Give the extent of all Plasmodium vivax-infected red blood cells.
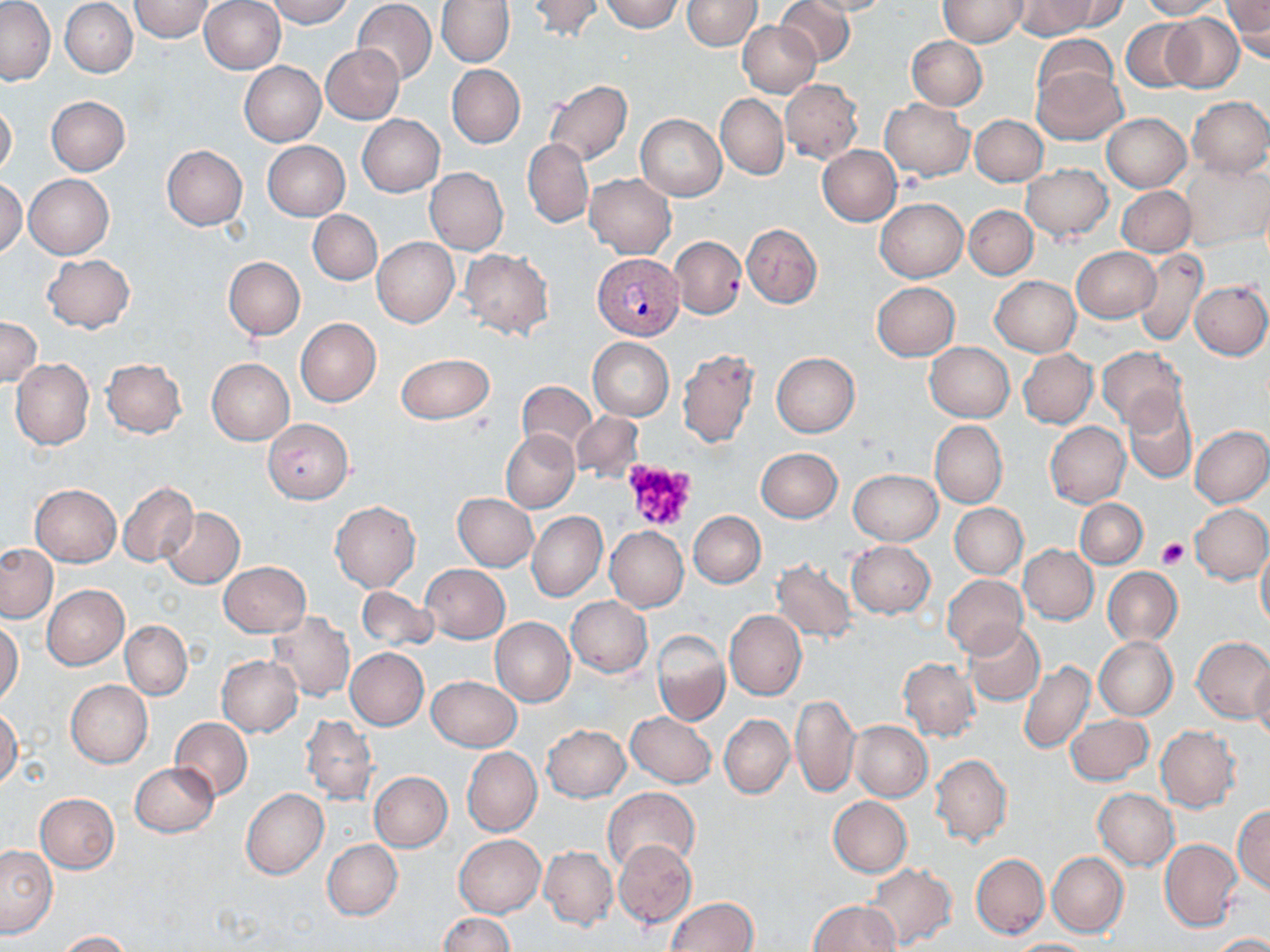
Approximate bounding boxes as (x1,y1)-(x2,y2) corner pairs in pixels.
Plasmodium vivax-infected red blood cells: (590,253)-(683,340).

slide_level_diagnosis: Plasmodium vivax
stain: May-Grünwald-Giemsa
image_size: 1270×952 pixels
preparation: thin blood smear
field_of_view: single
uninfected_red_blood_cell_locations: 'approximate bounding boxes as (x1,y1)-(x2,y2) corner pairs in pixels: (60,0)-(138,77), (128,0)-(215,42), (200,0)-(285,74), (266,0)-(354,27), (529,0)-(603,40), (598,0)-(684,32), (682,0)-(761,50), (774,0)-(854,66), (797,0)-(893,16), (1045,0)-(1132,33), (1136,0)-(1224,20), (1,1)-(55,84), (352,1)-(436,86), (436,1)-(514,67), (938,1)-(1027,47), (1012,1)-(1100,39), (1224,1)-(1270,61), (1161,13)-(1245,93), (1121,19)-(1199,93), (738,22)-(821,98), (1033,34)-(1119,112), (907,36)-(987,110), (321,44)-(404,123), (239,62)-(325,146), (447,64)-(525,149), (1031,66)-(1126,144), (781,80)-(863,163), (544,81)-(633,165), (716,94)-(789,179), (45,95)-(130,176), (1186,96)-(1270,178), (0,99)-(17,181), (880,99)-(973,180), (1102,113)-(1191,192), (970,114)-(1048,185), (357,115)-(444,196), (635,115)-(726,200), (522,139)-(594,228), (263,141)-(349,220), (161,145)-(247,230), (818,146)-(902,226), (1182,161)-(1269,250), (1023,164)-(1112,241), (425,168)-(508,254), (23,174)-(114,259), (584,174)-(676,259), (0,179)-(26,258), (1117,185)-(1196,255), (875,198)-(967,282), (964,206)-(1038,279), (308,210)-(382,284), (742,224)-(822,309), (669,236)-(746,319), (372,237)-(459,327), (1072,246)-(1159,321), (460,248)-(554,339), (1133,248)-(1208,346), (42,254)-(135,332), (223,256)-(305,340), (991,275)-(1081,356), (1189,281)-(1270,359), (871,282)-(960,360), (0,318)-(42,387), (295,318)-(381,406), (588,337)-(674,420), (925,342)-(1014,421), (1097,345)-(1189,430), (677,349)-(759,448), (1018,349)-(1098,428), (771,352)-(859,437), (396,353)-(495,424), (11,358)-(94,450), (100,358)-(187,437), (207,358)-(293,444), (516,380)-(596,457), (1123,388)-(1199,484), (571,411)-(645,482), (263,418)-(354,503), (931,420)-(1007,508), (1045,421)-(1130,507), (1190,425)-(1270,507), (501,430)-(580,513), (755,447)-(842,522), (848,469)-(941,544), (117,481)-(199,568), (30,484)-(121,566), (454,493)-(538,571), (1075,498)-(1147,568), (330,501)-(421,591), (950,503)-(1027,578), (1189,503)-(1270,584), (161,507)-(244,588), (528,511)-(607,602), (689,512)-(765,588), (605,526)-(687,612), (847,540)-(935,618), (1256,541)-(1270,632), (0,543)-(58,622), (1019,545)-(1098,625), (775,553)-(938,633), (771,560)-(858,643), (218,561)-(310,637), (421,565)-(510,642), (1102,567)-(1182,646), (943,574)-(1027,657), (41,585)-(129,670), (355,587)-(438,651), (566,596)-(652,677), (725,610)-(807,699), (268,612)-(355,701), (490,617)-(575,706), (1,619)-(23,707), (121,621)-(192,699), (964,623)-(1044,706), (652,631)-(729,726), (1093,636)-(1178,720), (1191,636)-(1270,723), (345,647)-(429,729), (217,655)-(303,736), (898,658)-(979,740), (1018,659)-(1095,754), (1252,662)-(1270,746), (427,675)-(521,752), (66,680)-(153,768), (790,694)-(859,798), (0,707)-(22,788), (626,712)-(716,787), (720,714)-(794,798), (1066,714)-(1153,786), (301,716)-(379,805), (169,717)-(253,801), (850,720)-(932,801), (542,724)-(630,801), (1155,725)-(1241,812), (463,747)-(542,836), (931,753)-(1012,846), (130,761)-(219,837), (369,772)-(452,852), (603,787)-(699,875), (241,788)-(328,879), (1093,788)-(1179,871), (36,794)-(119,874), (828,797)-(911,877), (1234,803)-(1270,895), (455,834)-(546,917), (323,839)-(402,921), (614,840)-(697,928), (1160,840)-(1242,931), (0,845)-(57,938), (539,846)-(618,929), (1048,851)-(1128,936), (971,854)-(1049,937), (865,864)-(958,950), (665,897)-(757,952), (808,901)-(900,952), (439,913)-(513,952), (58,930)-(134,951), (1206,932)-(1270,951), (1007,939)-(1099,951)'
modality: optical microscopy
platelet_locations: 'approximate bounding boxes as (x1,y1)-(x2,y2) corner pairs in pixels: (621,458)-(699,532), (1155,536)-(1191,569)'
magnification: 1000x